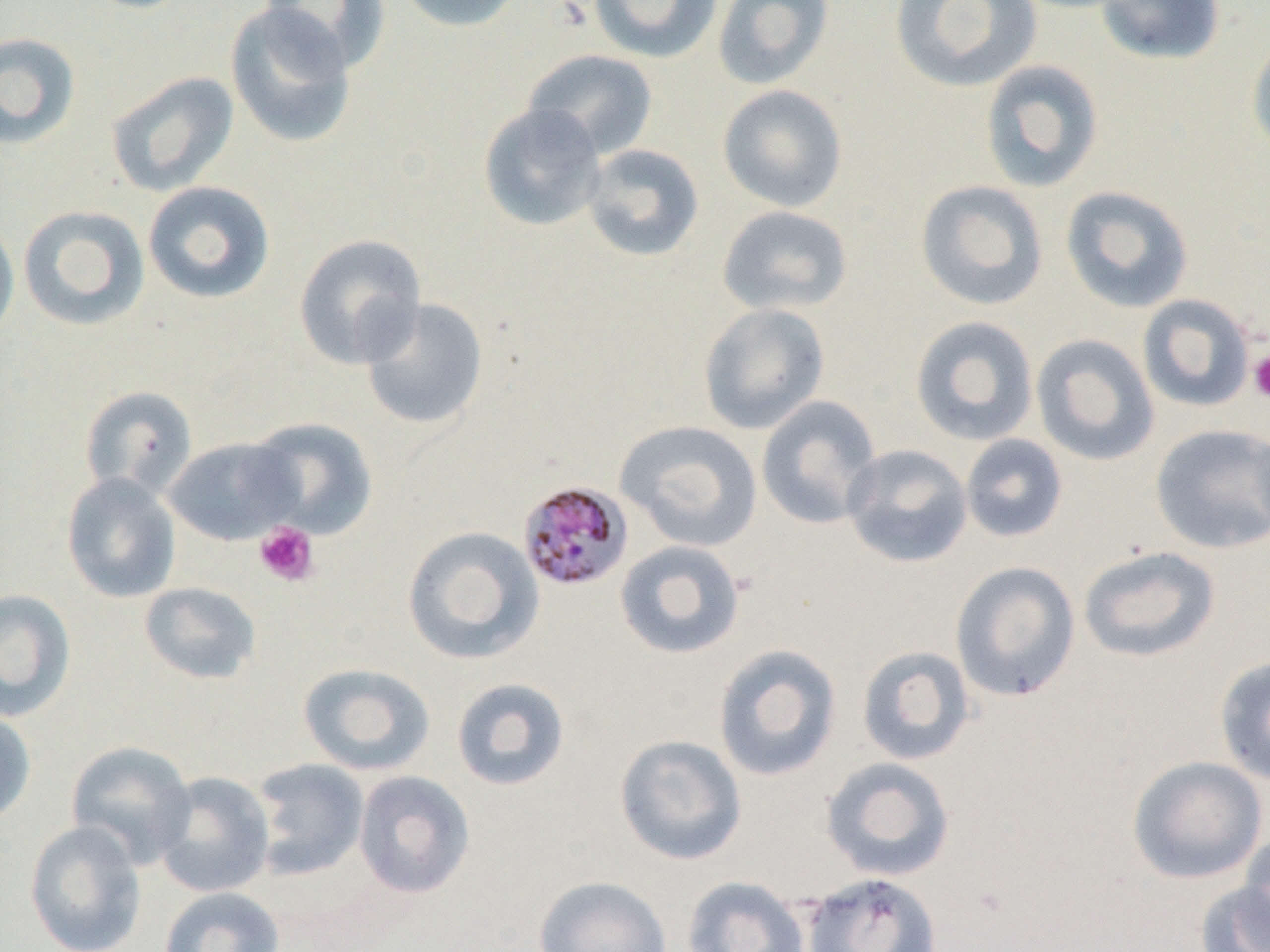 Approximate bounding boxes as named x1/y1/x2/y2 corners in pixels. Platelet locations: (x1=1248, y1=350, x2=1270, y2=402), (x1=254, y1=521, x2=319, y2=587). Uninfected red blood cell locations: (x1=77, y1=0, x2=197, y2=14), (x1=257, y1=0, x2=392, y2=72), (x1=392, y1=0, x2=524, y2=33), (x1=588, y1=0, x2=723, y2=63), (x1=712, y1=0, x2=834, y2=90), (x1=890, y1=0, x2=1043, y2=94), (x1=1095, y1=0, x2=1226, y2=66), (x1=224, y1=2, x2=359, y2=150), (x1=0, y1=31, x2=81, y2=149), (x1=1247, y1=31, x2=1270, y2=157), (x1=522, y1=49, x2=658, y2=160), (x1=979, y1=60, x2=1104, y2=193), (x1=105, y1=71, x2=239, y2=197), (x1=717, y1=83, x2=849, y2=213), (x1=478, y1=103, x2=607, y2=232), (x1=582, y1=144, x2=704, y2=262), (x1=915, y1=179, x2=1048, y2=311), (x1=142, y1=180, x2=276, y2=305), (x1=1060, y1=185, x2=1194, y2=313), (x1=17, y1=205, x2=150, y2=331), (x1=716, y1=205, x2=854, y2=316), (x1=0, y1=216, x2=19, y2=347), (x1=293, y1=233, x2=428, y2=369), (x1=1137, y1=294, x2=1256, y2=412), (x1=360, y1=297, x2=490, y2=431), (x1=698, y1=302, x2=831, y2=435), (x1=909, y1=315, x2=1039, y2=446), (x1=1030, y1=334, x2=1160, y2=467), (x1=79, y1=385, x2=197, y2=500), (x1=756, y1=395, x2=882, y2=529), (x1=245, y1=417, x2=379, y2=541), (x1=615, y1=420, x2=763, y2=552), (x1=1150, y1=423, x2=1270, y2=554), (x1=960, y1=434, x2=1068, y2=543), (x1=163, y1=436, x2=303, y2=546), (x1=841, y1=444, x2=973, y2=568), (x1=61, y1=471, x2=181, y2=603), (x1=402, y1=526, x2=544, y2=665), (x1=614, y1=539, x2=746, y2=659), (x1=1078, y1=546, x2=1221, y2=663), (x1=950, y1=561, x2=1081, y2=702), (x1=138, y1=581, x2=262, y2=685), (x1=0, y1=588, x2=77, y2=721), (x1=713, y1=643, x2=842, y2=781), (x1=857, y1=645, x2=976, y2=766), (x1=1214, y1=654, x2=1270, y2=787), (x1=298, y1=662, x2=435, y2=776), (x1=451, y1=677, x2=571, y2=791), (x1=0, y1=707, x2=37, y2=827), (x1=614, y1=733, x2=747, y2=865), (x1=66, y1=740, x2=197, y2=869), (x1=1127, y1=755, x2=1267, y2=884), (x1=820, y1=756, x2=956, y2=882), (x1=251, y1=758, x2=370, y2=880), (x1=353, y1=770, x2=475, y2=899), (x1=152, y1=771, x2=275, y2=898), (x1=24, y1=820, x2=147, y2=952), (x1=1238, y1=831, x2=1270, y2=944), (x1=801, y1=871, x2=943, y2=952), (x1=532, y1=875, x2=673, y2=952), (x1=681, y1=875, x2=809, y2=952), (x1=1195, y1=881, x2=1270, y2=952), (x1=159, y1=886, x2=285, y2=952). Plasmodium malariae-infected red blood cell locations: (x1=516, y1=480, x2=634, y2=592). Slide-level diagnosis: Plasmodium malariae. Image is 1270×952 pixels. Optical microscopy. Captured at 1000x magnification. Thin blood film. One field of a larger specimen.